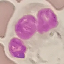

Result: no malaria parasites seen. Acquired by smartphone through the microscope eyepiece. Thin blood film. Cell patch, automatically extracted from a larger field of view and resized to 64 × 64 pixels. Giemsa-stained preparation.